Give the position of every Plasmodium parasite visible.
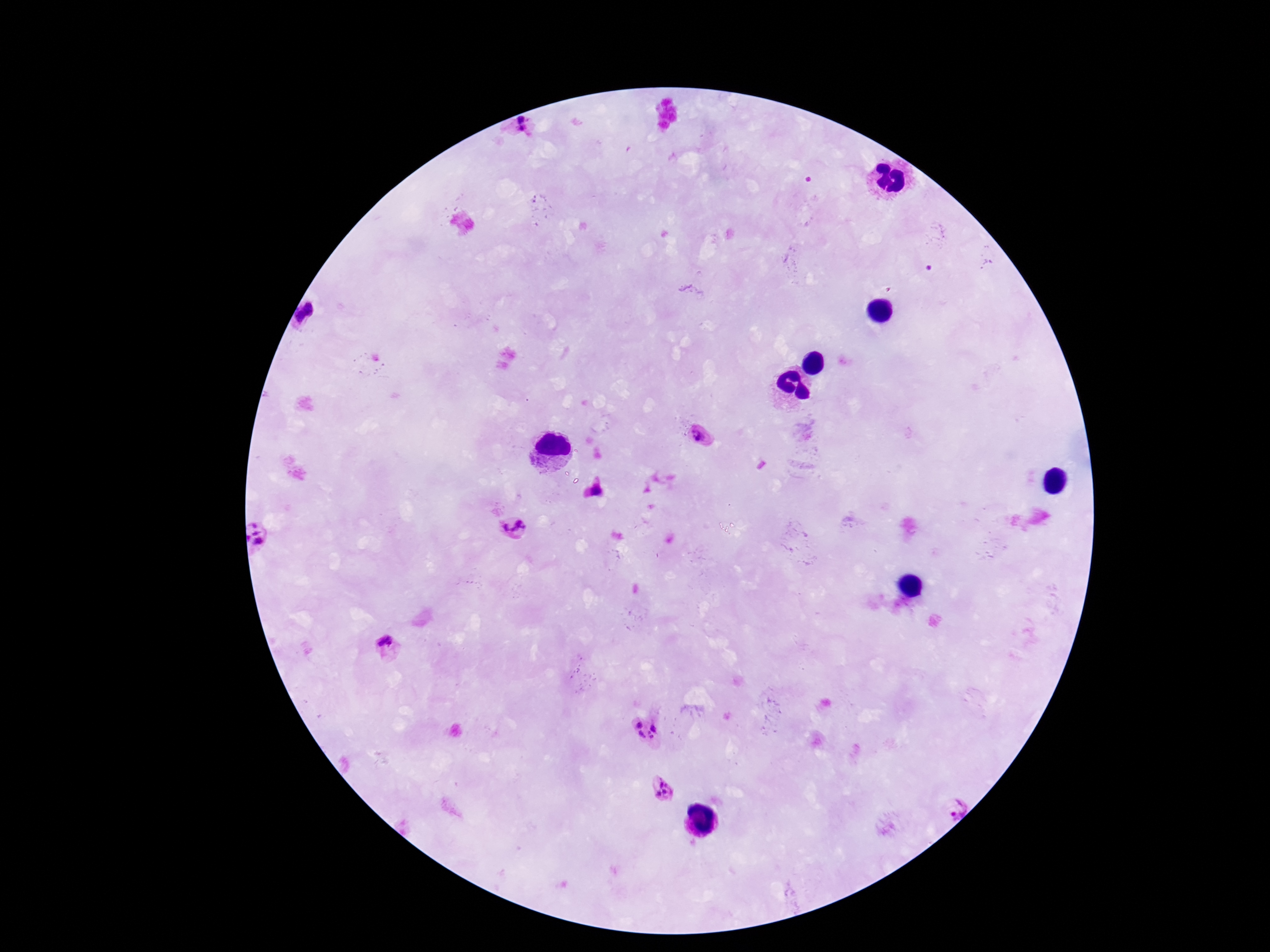
Approximate centers as [x, y] in pixels.
Plasmodium parasites: [524, 128], [310, 317], [702, 436], [596, 491], [513, 528], [261, 537], [385, 642], [640, 725], [656, 727], [643, 735], [650, 735], [662, 789], [954, 805].

Thick peripheral-blood smear. Image is 1270×952 pixels. Patient malaria status: positive. Smartphone photograph taken through the microscope eyepiece. One field from this slide. Giemsa stain. 100x magnification.